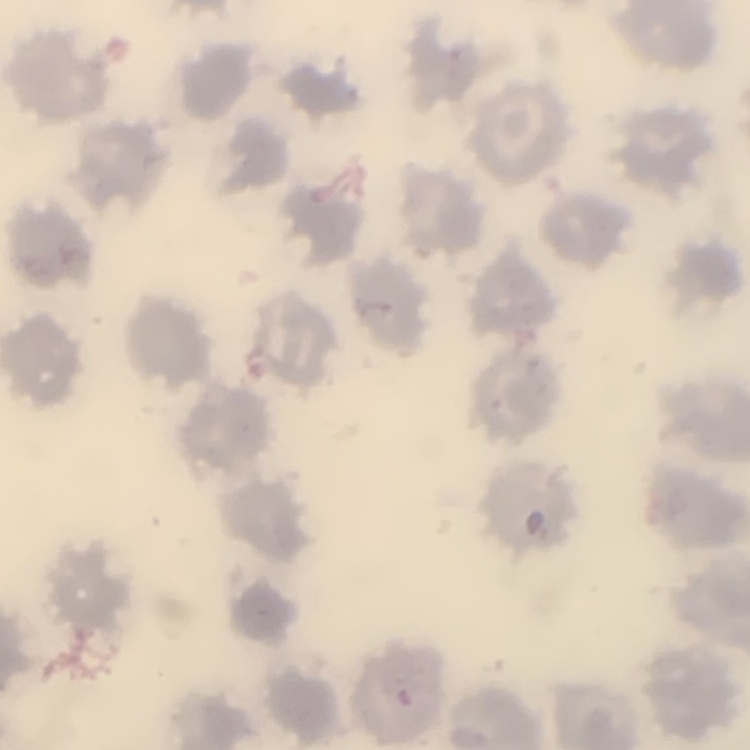
erythrocyte morphology = no rouleaux formation
stain = Field's or Giemsa
image type = one tile cut from a larger photomicrograph
preparation = thin blood film